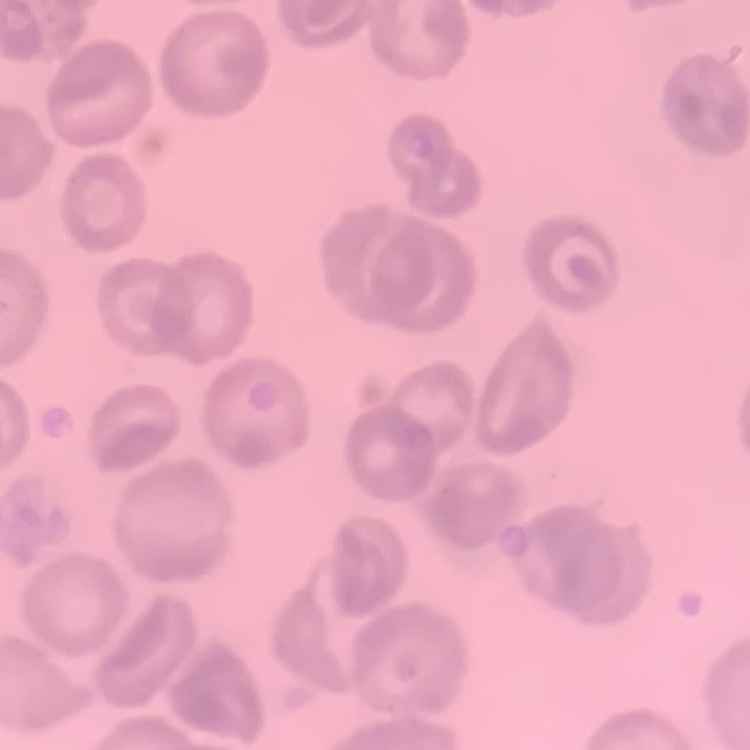
The erythrocytes exhibit no rouleaux formation. One tile cut from a larger photomicrograph. Thin blood film. Field's or Giemsa stain.